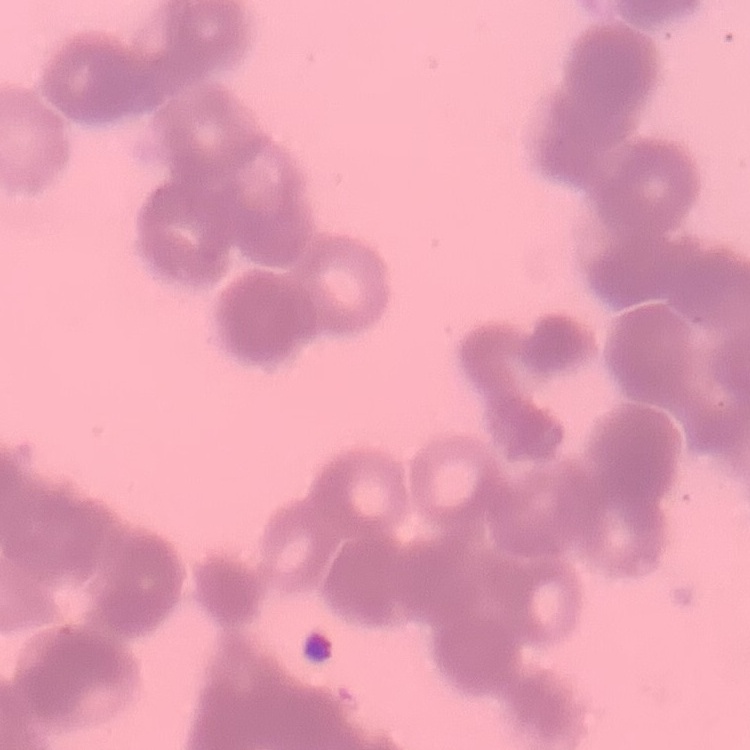

erythrocyte morphology = rouleaux formation
preparation = thin peripheral smear
stain = Field's or Giemsa
image type = square crop of a larger photomicrograph